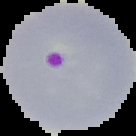

Summary:
  - Result: malaria parasites identified
  - Image size: 136×136 pixels
  - Image type: segmented cell region with the area outside set to black
  - Preparation: thin blood smear